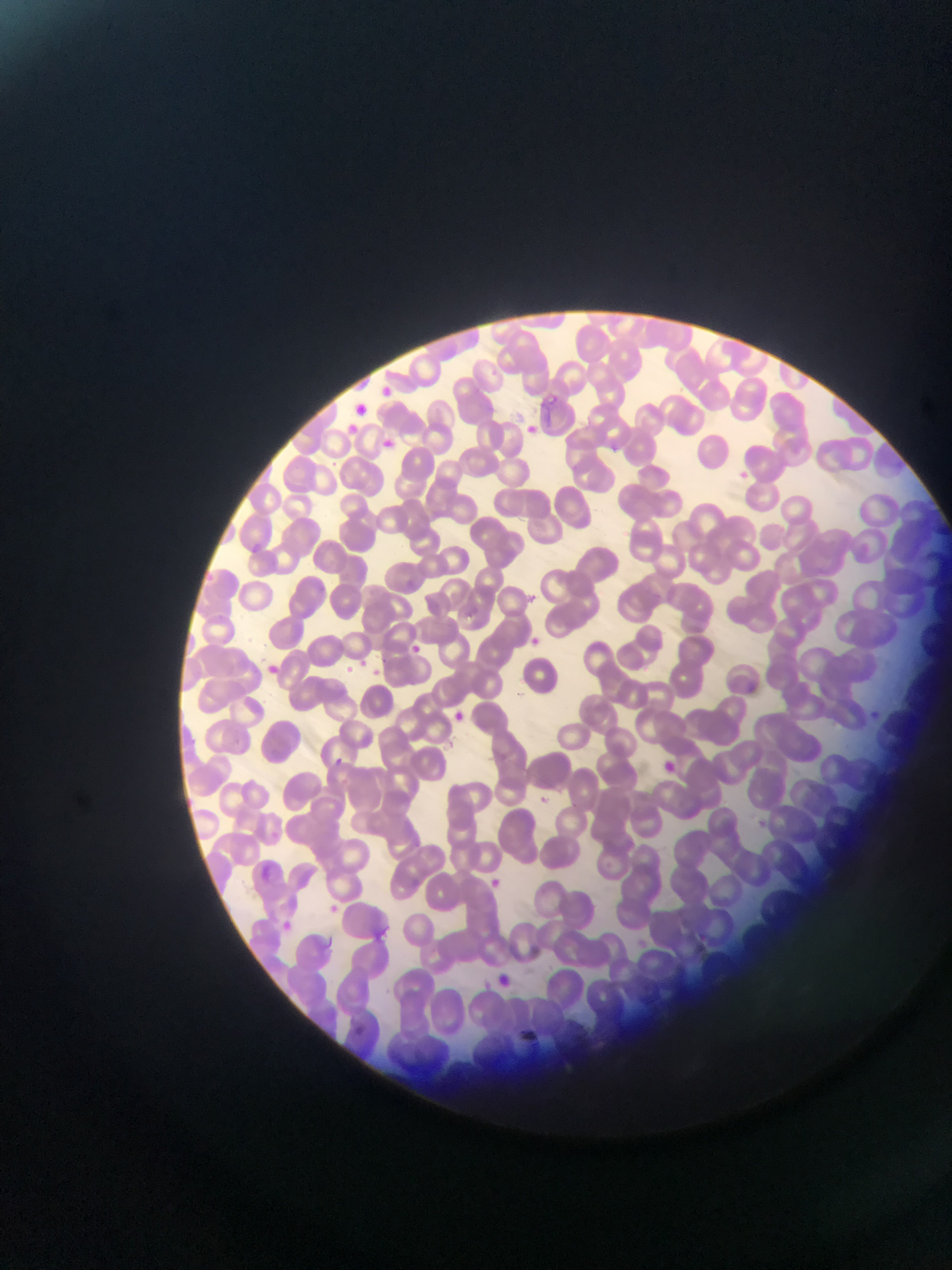

Approximate bounding boxes as [left, top, right, bottom] in pixels.
Summary:
  - Plasmodium parasite locations: [375, 382, 397, 402], [349, 399, 371, 419], [525, 421, 541, 435], [377, 435, 398, 454], [522, 632, 544, 651], [404, 641, 428, 661], [340, 662, 357, 678], [373, 667, 383, 680], [445, 707, 470, 729], [330, 753, 348, 769], [654, 755, 679, 778], [533, 792, 553, 809], [252, 865, 277, 887], [492, 875, 505, 889], [325, 902, 343, 920], [277, 918, 296, 935], [490, 970, 516, 991], [350, 1022, 369, 1039]
  - Capture: mobile-phone photograph through a microscope
  - Image size: 952×1270 pixels
  - Field of view: single
  - Preparation: thin blood film
  - Country: Ghana